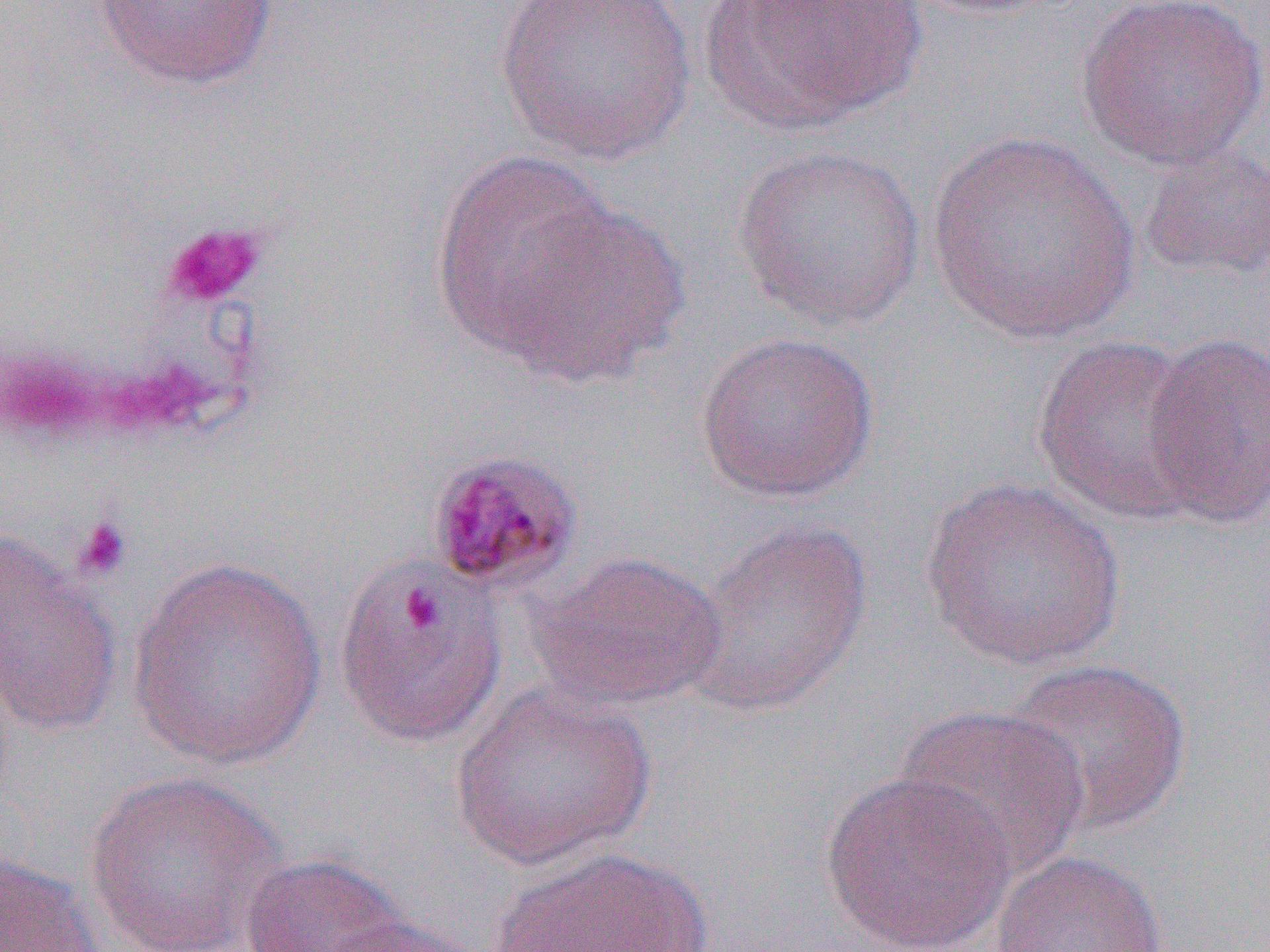
{
  "slide_level_diagnosis": "Plasmodium malariae",
  "uninfected_red_blood_cell_locations": "approximate bounding boxes as named x1/y1/x2/y2 corners in pixels: (x1=91, y1=0, x2=278, y2=91), (x1=494, y1=0, x2=697, y2=167), (x1=699, y1=0, x2=928, y2=135), (x1=1071, y1=0, x2=1270, y2=171), (x1=926, y1=130, x2=1141, y2=346), (x1=1137, y1=141, x2=1270, y2=284), (x1=732, y1=143, x2=928, y2=331), (x1=431, y1=148, x2=619, y2=364), (x1=491, y1=196, x2=689, y2=385), (x1=1142, y1=330, x2=1270, y2=527), (x1=694, y1=331, x2=880, y2=503), (x1=1032, y1=335, x2=1212, y2=527), (x1=919, y1=477, x2=1128, y2=672), (x1=679, y1=519, x2=873, y2=718), (x1=0, y1=534, x2=122, y2=738), (x1=530, y1=550, x2=727, y2=711), (x1=125, y1=556, x2=329, y2=769), (x1=332, y1=559, x2=507, y2=748), (x1=1001, y1=658, x2=1192, y2=837), (x1=451, y1=683, x2=657, y2=872), (x1=890, y1=703, x2=1092, y2=882), (x1=818, y1=769, x2=1017, y2=952), (x1=83, y1=771, x2=286, y2=952), (x1=488, y1=846, x2=716, y2=951), (x1=989, y1=849, x2=1169, y2=952), (x1=0, y1=851, x2=105, y2=951), (x1=239, y1=852, x2=412, y2=952), (x1=321, y1=916, x2=492, y2=952)",
  "image_size": "1270×952 pixels",
  "magnification": "1000x",
  "modality": "optical microscopy",
  "preparation": "thin blood smear",
  "field_of_view": "single",
  "platelet_locations_subset": "approximate bounding boxes as named x1/y1/x2/y2 corners in pixels: (x1=161, y1=220, x2=267, y2=309), (x1=71, y1=514, x2=132, y2=581)"
}